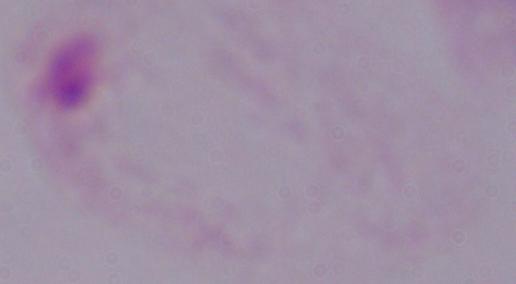
{
  "identification": "trichomonad",
  "modality": "photomicrograph",
  "magnification": "1000x"
}